Name the cell type shown.
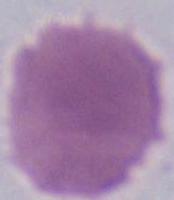

This is an erythrocyte.

Summary:
  - Modality: photomicrograph
  - Magnification: 1000x